Classify this cell by malaria status.
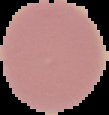
Uninfected.

Summary:
  - Image size: 109×115 pixels
  - Image type: segmented cell region with the area outside set to black
  - Preparation: thin blood smear